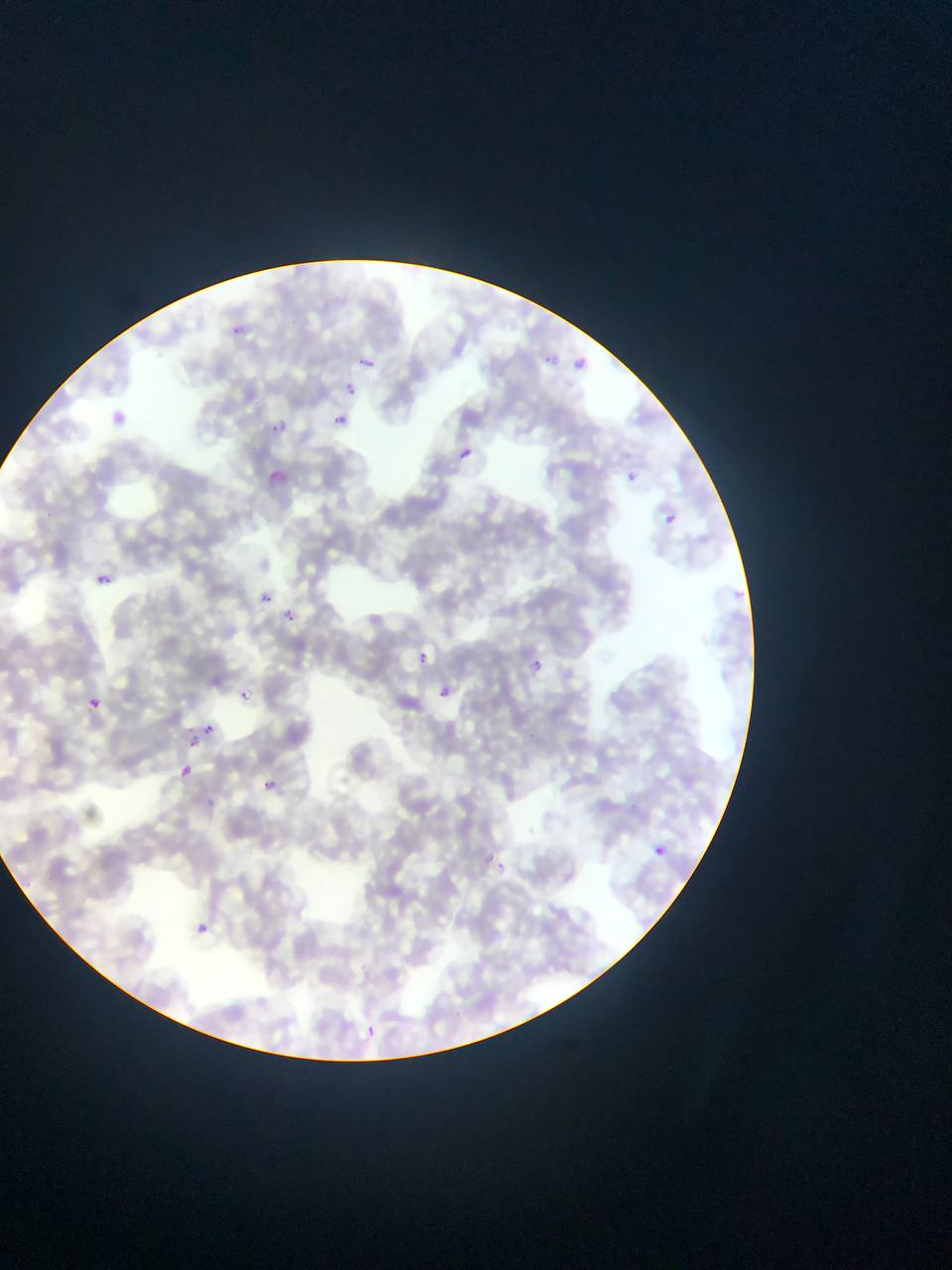

Approximate bounding boxes as [left, top, right, bottom] in pixels.
Summary:
  - Malaria parasite locations: [228, 319, 258, 349], [539, 344, 560, 372], [358, 353, 376, 373], [574, 355, 598, 378], [345, 380, 360, 397], [113, 402, 132, 425], [335, 411, 353, 428], [274, 414, 290, 432], [461, 445, 475, 460], [627, 464, 639, 487], [268, 465, 286, 478], [660, 508, 683, 532], [48, 510, 62, 526], [96, 573, 112, 585], [729, 588, 751, 607], [262, 592, 274, 604], [276, 610, 295, 625], [416, 650, 446, 679], [531, 658, 543, 673], [240, 690, 251, 700], [78, 691, 105, 708], [440, 691, 458, 710], [203, 724, 215, 734], [185, 730, 197, 746], [180, 763, 193, 777], [258, 776, 279, 799], [655, 847, 666, 855], [479, 855, 510, 878], [191, 920, 211, 937], [365, 1027, 383, 1047]
  - Country: Ghana
  - Capture: mobile-phone photograph through a microscope
  - Field of view: single
  - Image size: 952×1270 pixels
  - Preparation: thin blood film